Comment on the morphology of the erythrocytes.
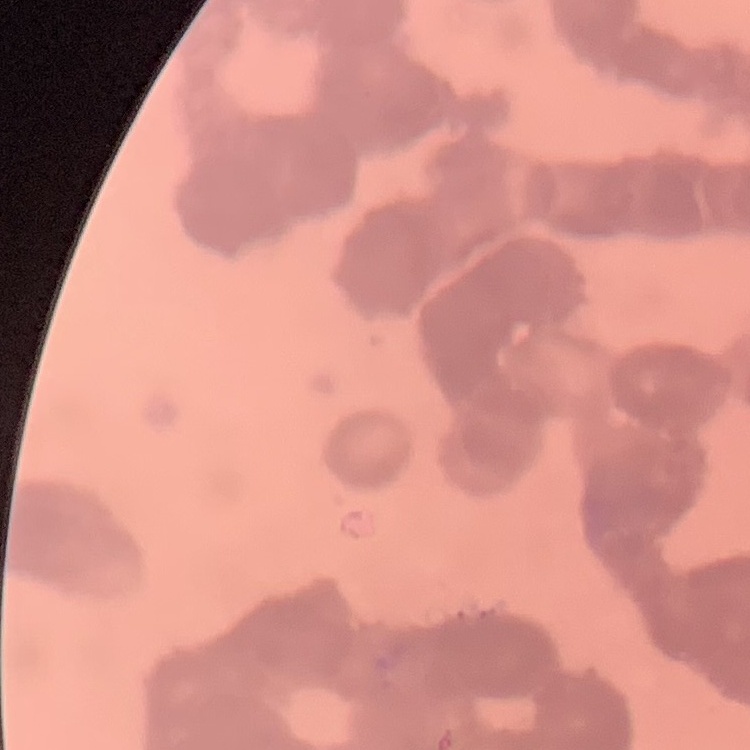
Rouleaux formation.

stain: Field's or Giemsa
preparation: thin blood film
image_type: one tile cut from a larger photomicrograph